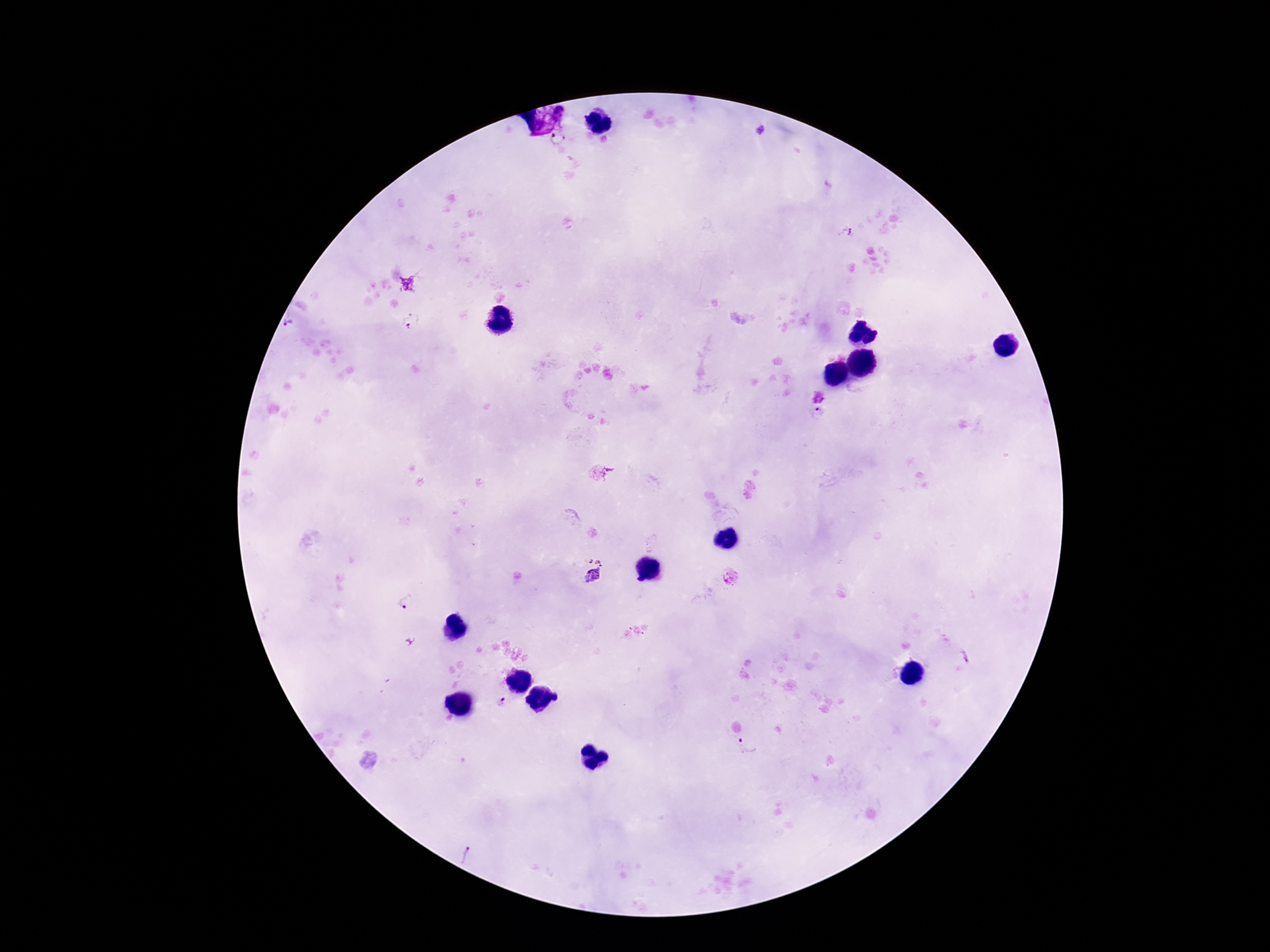
Approximate centers as [x, y] in pixels.
Summary:
  - Plasmodium parasite locations: [761, 130], [846, 233], [411, 320], [288, 324], [818, 413], [592, 571], [406, 603], [500, 702], [748, 745], [472, 855]
  - Patient malaria status: infected
  - Stain: Giemsa
  - Capture: smartphone camera through the microscope eyepiece
  - Preparation: thick blood film
  - Field of view: single
  - Magnification: 100x
  - Image size: 1270×952 pixels